Locate and identify every blood parasite.
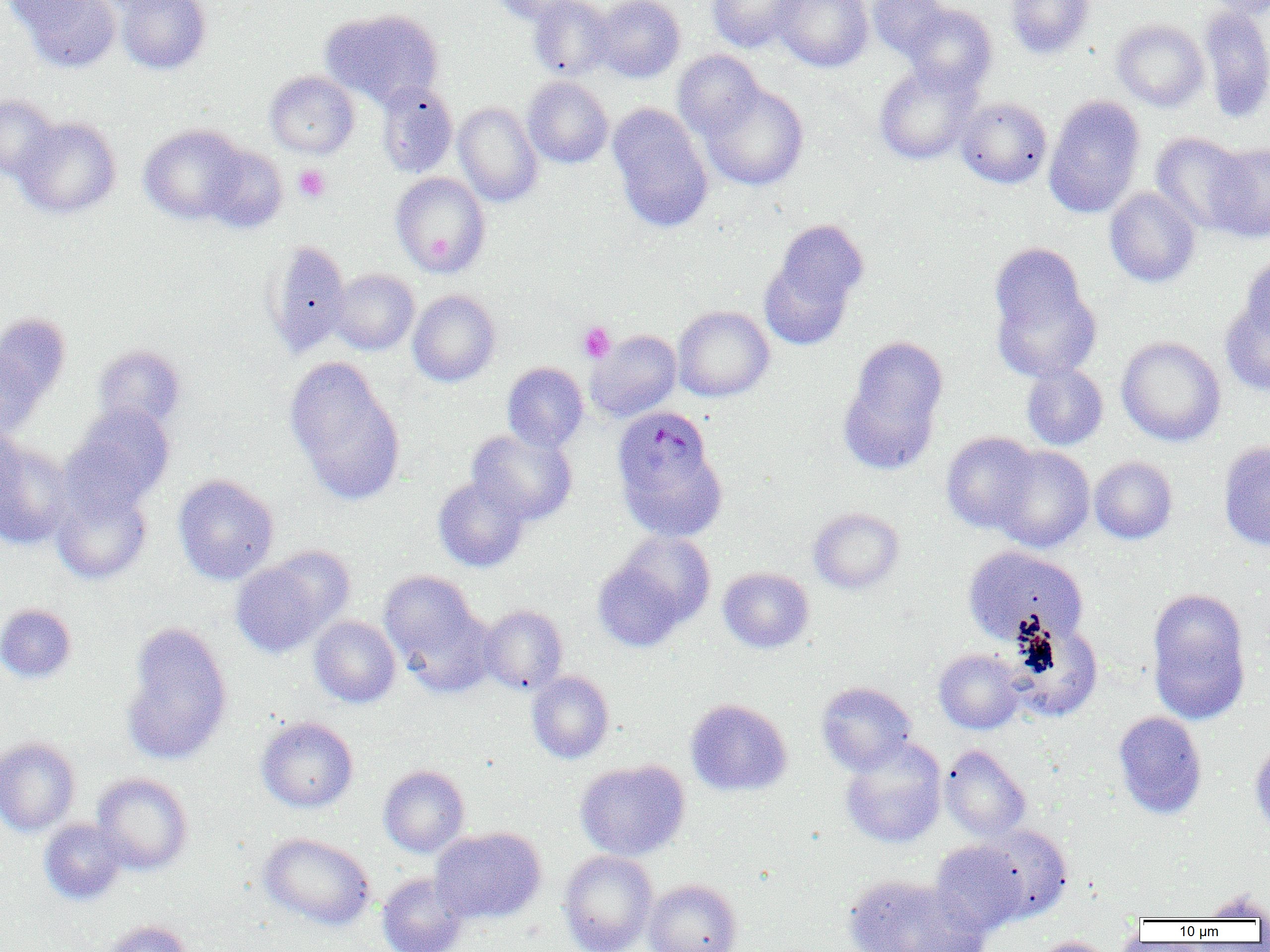

Approximate bounding boxes as (x1, y1, x2, y2) in pixels.
Plasmodium malariae-infected red blood cells: (612, 407, 716, 508).
No Plasmodium falciparum, Plasmodium ovale, Plasmodium vivax, Babesia divergens, or Trypanosoma brucei observed.

Summary:
  - Uninfected red blood cell locations: (12, 0, 121, 73), (116, 0, 211, 74), (489, 0, 581, 24), (528, 0, 614, 80), (593, 0, 685, 82), (707, 0, 806, 52), (773, 0, 873, 72), (867, 0, 950, 58), (1006, 0, 1095, 59), (1203, 0, 1270, 19), (902, 3, 998, 95), (1198, 6, 1270, 123), (320, 8, 443, 108), (1111, 19, 1209, 111), (672, 51, 765, 140), (874, 64, 980, 165), (264, 71, 359, 158), (523, 77, 613, 168), (376, 81, 458, 178), (700, 82, 809, 191), (0, 95, 60, 180), (1044, 96, 1146, 218), (956, 97, 1052, 189), (453, 102, 543, 206), (608, 106, 713, 232), (14, 116, 122, 219), (139, 124, 248, 224), (1150, 132, 1251, 234), (1203, 141, 1270, 242), (201, 144, 288, 232), (390, 172, 490, 278), (1104, 187, 1201, 288), (762, 220, 868, 346), (264, 240, 351, 357), (988, 248, 1099, 381), (1240, 252, 1269, 343), (330, 269, 419, 355), (408, 289, 501, 387), (1220, 297, 1270, 396), (672, 306, 774, 402), (1, 313, 71, 413), (586, 330, 682, 422), (1116, 336, 1226, 447), (839, 338, 948, 474), (0, 343, 47, 440), (93, 345, 186, 431), (284, 357, 406, 504), (502, 362, 588, 452), (1021, 364, 1108, 451), (65, 404, 175, 512), (0, 425, 26, 510), (467, 428, 577, 526), (941, 432, 1039, 534), (1218, 440, 1270, 552), (0, 443, 74, 550), (617, 443, 728, 542), (990, 445, 1095, 553), (1089, 456, 1178, 545), (173, 474, 279, 584), (433, 476, 529, 572), (50, 482, 153, 585), (808, 507, 904, 594), (593, 533, 715, 648), (963, 546, 1088, 646), (230, 554, 345, 657), (718, 567, 814, 653), (379, 570, 486, 679), (1147, 589, 1251, 723), (0, 603, 77, 684), (480, 605, 568, 694), (309, 616, 400, 707), (121, 621, 233, 765), (1009, 621, 1103, 721), (933, 648, 1027, 734), (527, 671, 614, 763), (816, 681, 917, 774), (685, 698, 792, 796), (1112, 711, 1208, 818), (257, 717, 358, 812), (1250, 735, 1270, 836), (0, 737, 80, 836), (840, 739, 947, 849), (940, 744, 1031, 841), (575, 759, 690, 860), (378, 765, 470, 857), (92, 773, 193, 875), (38, 818, 127, 905), (977, 824, 1073, 923), (431, 827, 546, 925), (258, 833, 376, 930), (930, 840, 1030, 936), (559, 850, 658, 952), (377, 873, 469, 952), (844, 874, 987, 952), (643, 879, 742, 952), (1196, 891, 1270, 921), (101, 920, 194, 952), (1029, 936, 1119, 952)
  - Platelet locations: (293, 164, 331, 202), (577, 322, 616, 363)
  - Slide-level diagnosis: Plasmodium malariae
  - Field of view: one of a larger specimen
  - Preparation: thin blood film
  - Magnification: 1000x
  - Modality: light microscopy
  - Image size: 1270×952 pixels